Assess this cell for malaria.
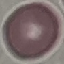
Uninfected.

{
  "capture": "smartphone camera at the microscope eyepiece",
  "image_type": "automatically extracted cell patch, resized to 64 × 64 pixels",
  "stain": "Giemsa",
  "preparation": "thin blood film"
}